Assess this cell for malaria.
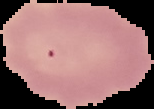

Uninfected.

Segmented cell region on a black background. From a thin blood smear. Image is 154×109 pixels.